State which parasite is depicted.
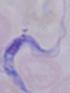

This is a trypanosome.

Captured at 1000x magnification. Micrograph.